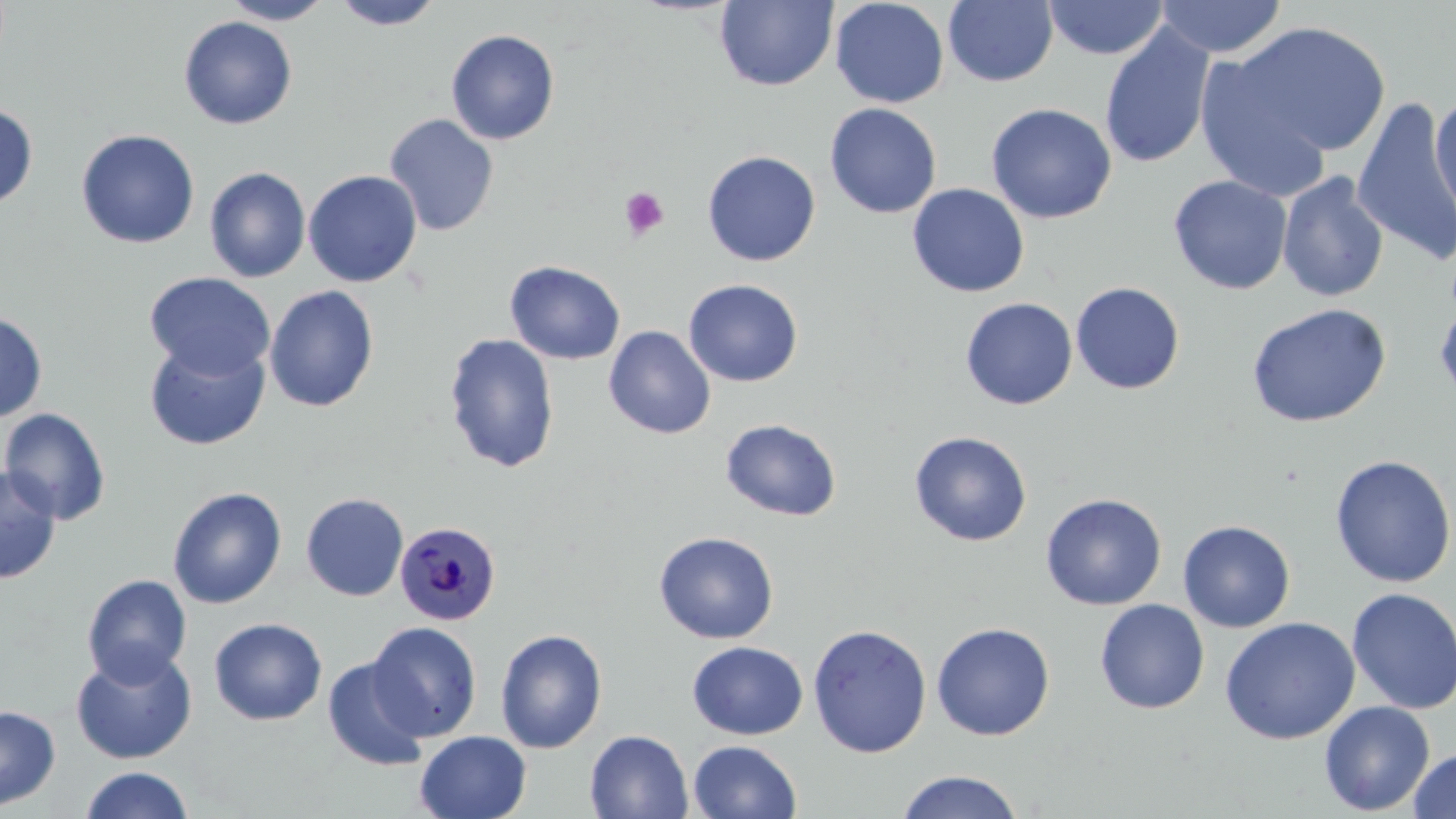
slide-level diagnosis = Plasmodium malariae
preparation = thin blood film
magnification = 1000x
stain = May-Grünwald-Giemsa
image size = 1456×819 pixels
Plasmodium malariae-infected red blood cell locations = approximate bounding boxes as named x1/y1/x2/y2 corners in pixels: (x1=394, y1=521, x2=501, y2=626)
uninfected red blood cell locations = approximate bounding boxes as named x1/y1/x2/y2 corners in pixels: (x1=221, y1=0, x2=334, y2=25), (x1=332, y1=0, x2=444, y2=30), (x1=830, y1=0, x2=949, y2=108), (x1=943, y1=0, x2=1058, y2=87), (x1=1043, y1=0, x2=1168, y2=60), (x1=1154, y1=0, x2=1287, y2=59), (x1=715, y1=1, x2=838, y2=91), (x1=178, y1=15, x2=299, y2=130), (x1=1230, y1=21, x2=1392, y2=159), (x1=1099, y1=23, x2=1216, y2=169), (x1=446, y1=29, x2=560, y2=145), (x1=1193, y1=48, x2=1337, y2=202), (x1=1429, y1=92, x2=1456, y2=225), (x1=1352, y1=97, x2=1456, y2=267), (x1=0, y1=102, x2=38, y2=210), (x1=824, y1=102, x2=942, y2=219), (x1=985, y1=102, x2=1117, y2=224), (x1=383, y1=113, x2=499, y2=236), (x1=76, y1=129, x2=200, y2=249), (x1=702, y1=150, x2=821, y2=266), (x1=204, y1=166, x2=312, y2=283), (x1=303, y1=169, x2=423, y2=287), (x1=1276, y1=171, x2=1389, y2=303), (x1=1168, y1=174, x2=1293, y2=295), (x1=907, y1=183, x2=1030, y2=298), (x1=504, y1=260, x2=626, y2=365), (x1=144, y1=271, x2=276, y2=380), (x1=683, y1=279, x2=804, y2=387), (x1=1070, y1=281, x2=1185, y2=395), (x1=264, y1=286, x2=380, y2=412), (x1=960, y1=297, x2=1078, y2=410), (x1=1434, y1=300, x2=1456, y2=411), (x1=1245, y1=303, x2=1391, y2=428), (x1=0, y1=311, x2=48, y2=423), (x1=604, y1=325, x2=716, y2=439), (x1=443, y1=333, x2=560, y2=474), (x1=144, y1=338, x2=270, y2=451), (x1=0, y1=406, x2=112, y2=525), (x1=720, y1=418, x2=842, y2=522), (x1=909, y1=430, x2=1032, y2=547), (x1=1330, y1=454, x2=1456, y2=588), (x1=0, y1=464, x2=62, y2=585), (x1=167, y1=487, x2=287, y2=609), (x1=300, y1=492, x2=409, y2=601), (x1=1040, y1=493, x2=1167, y2=610), (x1=1177, y1=520, x2=1296, y2=632), (x1=653, y1=530, x2=779, y2=644), (x1=81, y1=573, x2=192, y2=686), (x1=1347, y1=587, x2=1456, y2=715), (x1=1095, y1=599, x2=1209, y2=714), (x1=1219, y1=616, x2=1360, y2=745), (x1=208, y1=617, x2=327, y2=725), (x1=367, y1=622, x2=482, y2=741), (x1=931, y1=622, x2=1055, y2=741), (x1=807, y1=623, x2=933, y2=757), (x1=495, y1=628, x2=608, y2=753), (x1=687, y1=640, x2=808, y2=740), (x1=70, y1=646, x2=198, y2=765), (x1=322, y1=656, x2=431, y2=772), (x1=1319, y1=700, x2=1435, y2=815), (x1=0, y1=705, x2=60, y2=811), (x1=414, y1=730, x2=532, y2=819), (x1=585, y1=730, x2=693, y2=819), (x1=688, y1=740, x2=802, y2=819), (x1=1407, y1=748, x2=1456, y2=819), (x1=78, y1=766, x2=196, y2=819), (x1=895, y1=769, x2=1025, y2=819)
platelet locations = approximate bounding boxes as named x1/y1/x2/y2 corners in pixels: (x1=618, y1=186, x2=670, y2=240)
field of view = single
modality = light microscopy